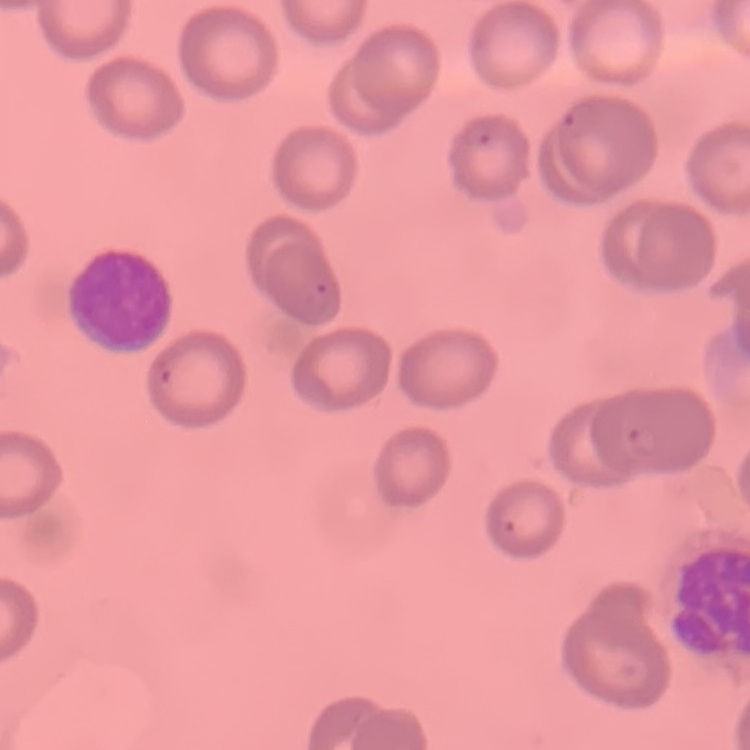
red blood cell morphology = no rouleaux formation
stain = Field's or Giemsa
image type = one tile cut from a larger photomicrograph
preparation = thin blood film